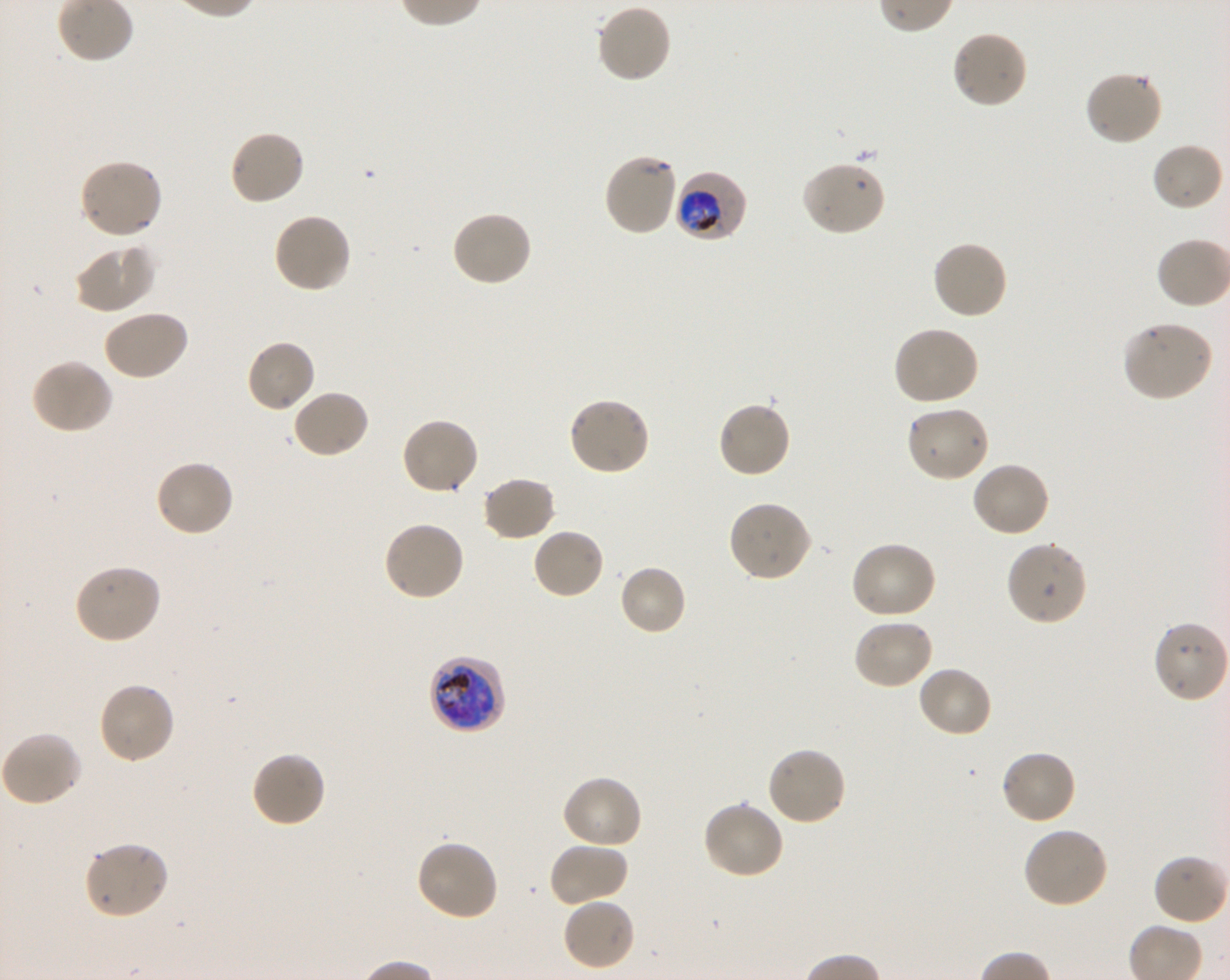

Approximate bounding rectangles given as corner coordinates in pixels from the top-left. Not every red blood cell is marked. A life-cycle stage — or a range of stages, where the recorded stages span more than one — follows each staged infected red blood cell.
Summary:
  - Locations of uninfected red blood cells: (x1=595, y1=3, x2=672, y2=84), (x1=951, y1=30, x2=1028, y2=110), (x1=1083, y1=70, x2=1163, y2=147), (x1=228, y1=129, x2=306, y2=207), (x1=1150, y1=142, x2=1225, y2=214), (x1=603, y1=152, x2=680, y2=237), (x1=78, y1=159, x2=164, y2=240), (x1=800, y1=161, x2=888, y2=237), (x1=450, y1=210, x2=534, y2=287), (x1=271, y1=211, x2=353, y2=295), (x1=932, y1=239, x2=1009, y2=320), (x1=73, y1=244, x2=155, y2=313), (x1=101, y1=309, x2=189, y2=382), (x1=1121, y1=320, x2=1215, y2=402), (x1=892, y1=325, x2=980, y2=406), (x1=245, y1=338, x2=316, y2=414), (x1=30, y1=357, x2=114, y2=434), (x1=290, y1=389, x2=371, y2=460), (x1=567, y1=395, x2=652, y2=476), (x1=716, y1=400, x2=792, y2=479), (x1=904, y1=406, x2=991, y2=483), (x1=400, y1=416, x2=480, y2=496), (x1=153, y1=459, x2=235, y2=538), (x1=971, y1=461, x2=1051, y2=538), (x1=481, y1=476, x2=557, y2=542), (x1=727, y1=501, x2=813, y2=583), (x1=383, y1=520, x2=466, y2=603), (x1=531, y1=527, x2=606, y2=600), (x1=1005, y1=539, x2=1088, y2=626), (x1=850, y1=541, x2=937, y2=621), (x1=72, y1=562, x2=162, y2=646), (x1=618, y1=564, x2=688, y2=637), (x1=852, y1=617, x2=935, y2=690), (x1=1153, y1=620, x2=1229, y2=704), (x1=917, y1=664, x2=994, y2=738), (x1=96, y1=680, x2=176, y2=766), (x1=1, y1=731, x2=84, y2=807), (x1=765, y1=747, x2=848, y2=827), (x1=998, y1=749, x2=1077, y2=826), (x1=251, y1=750, x2=327, y2=828), (x1=561, y1=774, x2=644, y2=850), (x1=701, y1=799, x2=785, y2=881), (x1=1021, y1=826, x2=1110, y2=909), (x1=415, y1=839, x2=500, y2=923), (x1=83, y1=840, x2=170, y2=921), (x1=548, y1=841, x2=628, y2=908), (x1=561, y1=897, x2=636, y2=972)
  - Locations of infected red blood cells: (x1=673, y1=171, x2=748, y2=243) trophozoite; (x1=428, y1=654, x2=506, y2=735) late trophozoite to late schizont
  - Donor blood group: O+
  - Field of view: single
  - Stain: Giemsa
  - Culture: Plasmodium falciparum strain 3D7, shaking, in vitro
  - Objective: 100x, oil immersion, numerical aperture 1.30
  - Image size: 1230×980 pixels
  - Preparation: thin blood smear